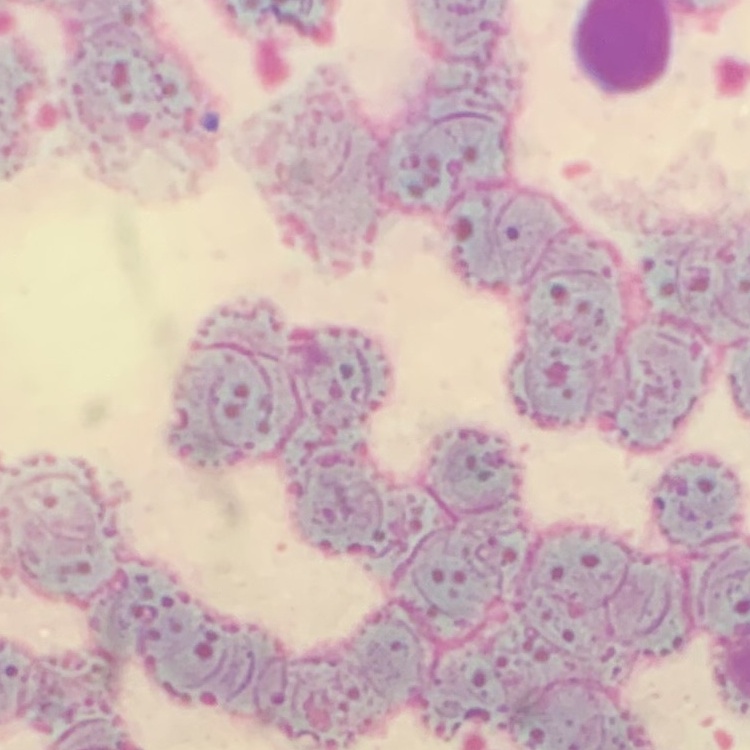
erythrocyte morphology = rouleaux formation
stain = Field's or Giemsa
preparation = thin blood smear
image type = one tile cut from a larger photomicrograph